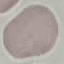

Summary:
  - Malaria status: uninfected
  - Preparation: thin blood film
  - Image type: cell patch, automatically extracted from a larger field of view and resized to 64 × 64 pixels
  - Stain: Giemsa
  - Capture: smartphone camera at the microscope eyepiece